Report the malaria status of this cell.
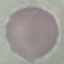

Uninfected.

capture = smartphone camera at the microscope eyepiece
stain = Giemsa
image type = cell patch, automatically extracted from a larger field of view and resized to 64 × 64 pixels
preparation = thin blood film